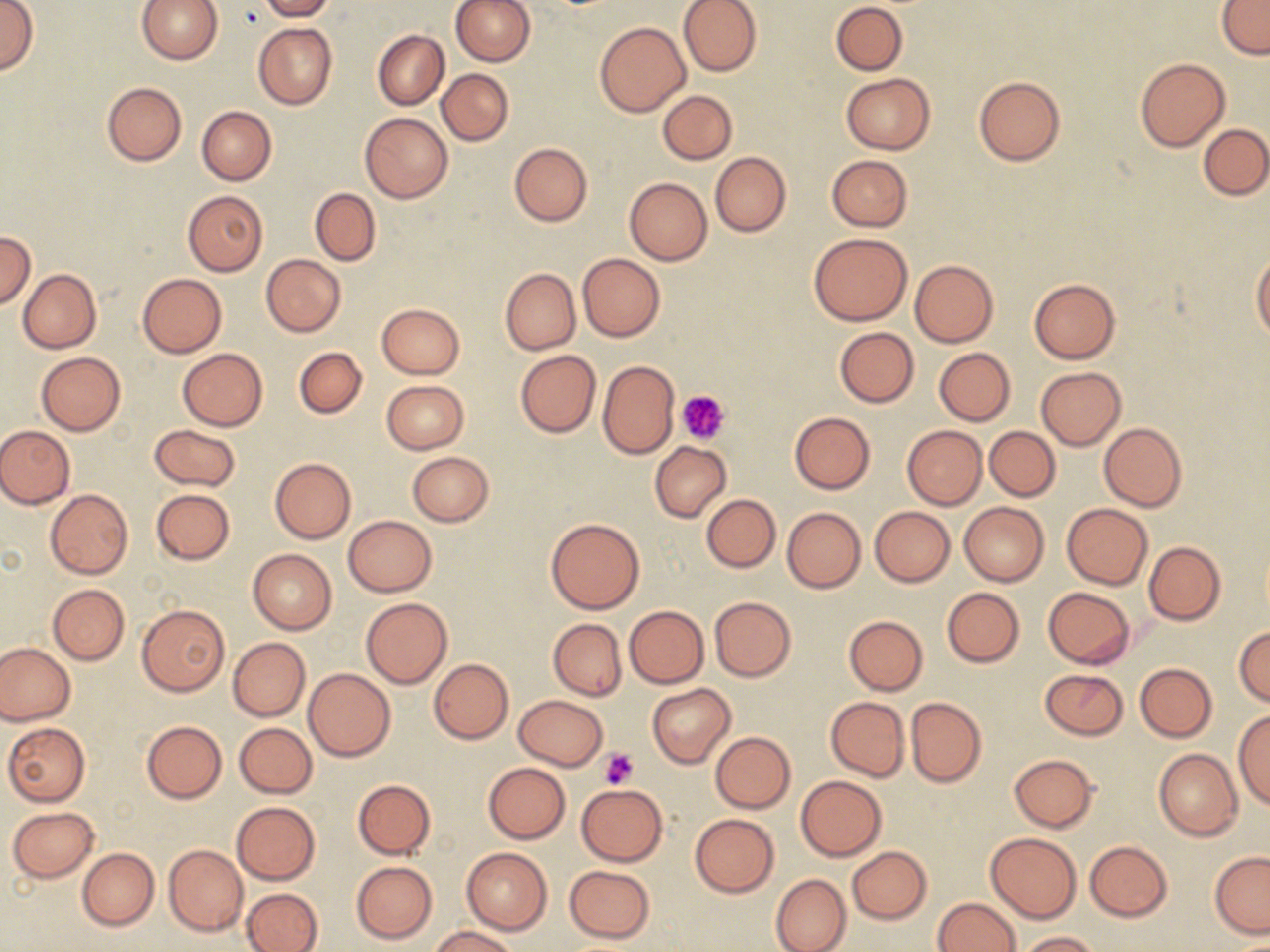
slide-level diagnosis = negative for blood parasites
field of view = one of a larger specimen
platelet locations = approximate bounding boxes as named x1/y1/x2/y2 corners in pixels: (x1=678, y1=389, x2=730, y2=445), (x1=599, y1=748, x2=639, y2=790)
image size = 1270×952 pixels
stain = May-Grünwald-Giemsa
uninfected red blood cell locations = approximate bounding boxes as named x1/y1/x2/y2 corners in pixels: (x1=0, y1=0, x2=37, y2=76), (x1=135, y1=0, x2=222, y2=65), (x1=259, y1=0, x2=334, y2=20), (x1=451, y1=0, x2=535, y2=65), (x1=678, y1=0, x2=762, y2=76), (x1=1217, y1=0, x2=1269, y2=57), (x1=830, y1=2, x2=907, y2=75), (x1=594, y1=20, x2=691, y2=117), (x1=253, y1=23, x2=337, y2=110), (x1=373, y1=30, x2=449, y2=110), (x1=1134, y1=57, x2=1230, y2=152), (x1=437, y1=69, x2=514, y2=145), (x1=841, y1=74, x2=934, y2=154), (x1=974, y1=76, x2=1065, y2=166), (x1=102, y1=82, x2=187, y2=166), (x1=657, y1=89, x2=737, y2=165), (x1=196, y1=107, x2=276, y2=185), (x1=360, y1=113, x2=454, y2=203), (x1=1199, y1=124, x2=1270, y2=200), (x1=509, y1=143, x2=592, y2=226), (x1=710, y1=151, x2=791, y2=237), (x1=827, y1=154, x2=913, y2=230), (x1=624, y1=178, x2=712, y2=265), (x1=310, y1=188, x2=381, y2=265), (x1=183, y1=190, x2=268, y2=277), (x1=0, y1=230, x2=36, y2=310), (x1=808, y1=233, x2=913, y2=326), (x1=577, y1=253, x2=665, y2=341), (x1=1251, y1=253, x2=1270, y2=343), (x1=261, y1=254, x2=346, y2=337), (x1=909, y1=259, x2=998, y2=347), (x1=500, y1=268, x2=580, y2=355), (x1=19, y1=269, x2=101, y2=353), (x1=136, y1=273, x2=226, y2=357), (x1=1028, y1=277, x2=1122, y2=364), (x1=375, y1=302, x2=466, y2=379), (x1=834, y1=327, x2=919, y2=407), (x1=293, y1=346, x2=367, y2=418), (x1=178, y1=348, x2=268, y2=431), (x1=934, y1=348, x2=1015, y2=425), (x1=515, y1=350, x2=601, y2=438), (x1=36, y1=352, x2=125, y2=435), (x1=598, y1=360, x2=680, y2=459), (x1=1036, y1=367, x2=1126, y2=450), (x1=381, y1=380, x2=468, y2=454), (x1=788, y1=411, x2=875, y2=494), (x1=1100, y1=422, x2=1187, y2=511), (x1=149, y1=423, x2=240, y2=491), (x1=902, y1=425, x2=987, y2=509), (x1=0, y1=426, x2=75, y2=508), (x1=985, y1=426, x2=1060, y2=501), (x1=650, y1=441, x2=732, y2=522), (x1=406, y1=451, x2=494, y2=526), (x1=269, y1=458, x2=356, y2=543), (x1=151, y1=489, x2=234, y2=565), (x1=44, y1=490, x2=132, y2=579), (x1=701, y1=494, x2=780, y2=573), (x1=958, y1=502, x2=1049, y2=586), (x1=1060, y1=502, x2=1153, y2=590), (x1=869, y1=506, x2=955, y2=586), (x1=781, y1=507, x2=866, y2=594), (x1=342, y1=516, x2=436, y2=596), (x1=545, y1=517, x2=645, y2=614), (x1=1144, y1=540, x2=1226, y2=625), (x1=247, y1=549, x2=337, y2=634), (x1=47, y1=584, x2=129, y2=665), (x1=1042, y1=587, x2=1135, y2=668), (x1=941, y1=588, x2=1024, y2=668), (x1=710, y1=596, x2=797, y2=681), (x1=361, y1=597, x2=453, y2=688), (x1=136, y1=603, x2=231, y2=697), (x1=624, y1=605, x2=709, y2=688), (x1=843, y1=616, x2=927, y2=695), (x1=548, y1=618, x2=626, y2=700), (x1=1233, y1=626, x2=1270, y2=707), (x1=228, y1=637, x2=310, y2=721), (x1=0, y1=643, x2=75, y2=725), (x1=428, y1=658, x2=514, y2=744), (x1=1135, y1=662, x2=1218, y2=742), (x1=303, y1=668, x2=395, y2=761), (x1=1040, y1=668, x2=1128, y2=740), (x1=646, y1=684, x2=736, y2=768), (x1=513, y1=695, x2=607, y2=770), (x1=825, y1=696, x2=910, y2=781), (x1=905, y1=697, x2=986, y2=787), (x1=1233, y1=708, x2=1270, y2=810), (x1=141, y1=720, x2=228, y2=803), (x1=3, y1=722, x2=90, y2=806), (x1=233, y1=722, x2=317, y2=798), (x1=710, y1=732, x2=796, y2=812), (x1=1154, y1=748, x2=1244, y2=842), (x1=1009, y1=753, x2=1099, y2=832), (x1=483, y1=763, x2=570, y2=843), (x1=795, y1=775, x2=887, y2=861), (x1=352, y1=779, x2=435, y2=860), (x1=577, y1=784, x2=668, y2=865), (x1=231, y1=801, x2=321, y2=884), (x1=6, y1=805, x2=99, y2=883), (x1=690, y1=813, x2=780, y2=897), (x1=985, y1=832, x2=1082, y2=923), (x1=1084, y1=841, x2=1174, y2=922), (x1=164, y1=845, x2=248, y2=935), (x1=848, y1=846, x2=932, y2=924), (x1=77, y1=847, x2=159, y2=930), (x1=461, y1=847, x2=552, y2=934), (x1=1209, y1=851, x2=1270, y2=938), (x1=351, y1=861, x2=437, y2=943), (x1=563, y1=864, x2=655, y2=943), (x1=771, y1=873, x2=851, y2=952), (x1=241, y1=888, x2=324, y2=952), (x1=933, y1=897, x2=1020, y2=952), (x1=428, y1=925, x2=521, y2=951), (x1=1020, y1=930, x2=1098, y2=951)
preparation = thin blood film
magnification = 1000x
modality = light microscopy